Point out each leukocyte.
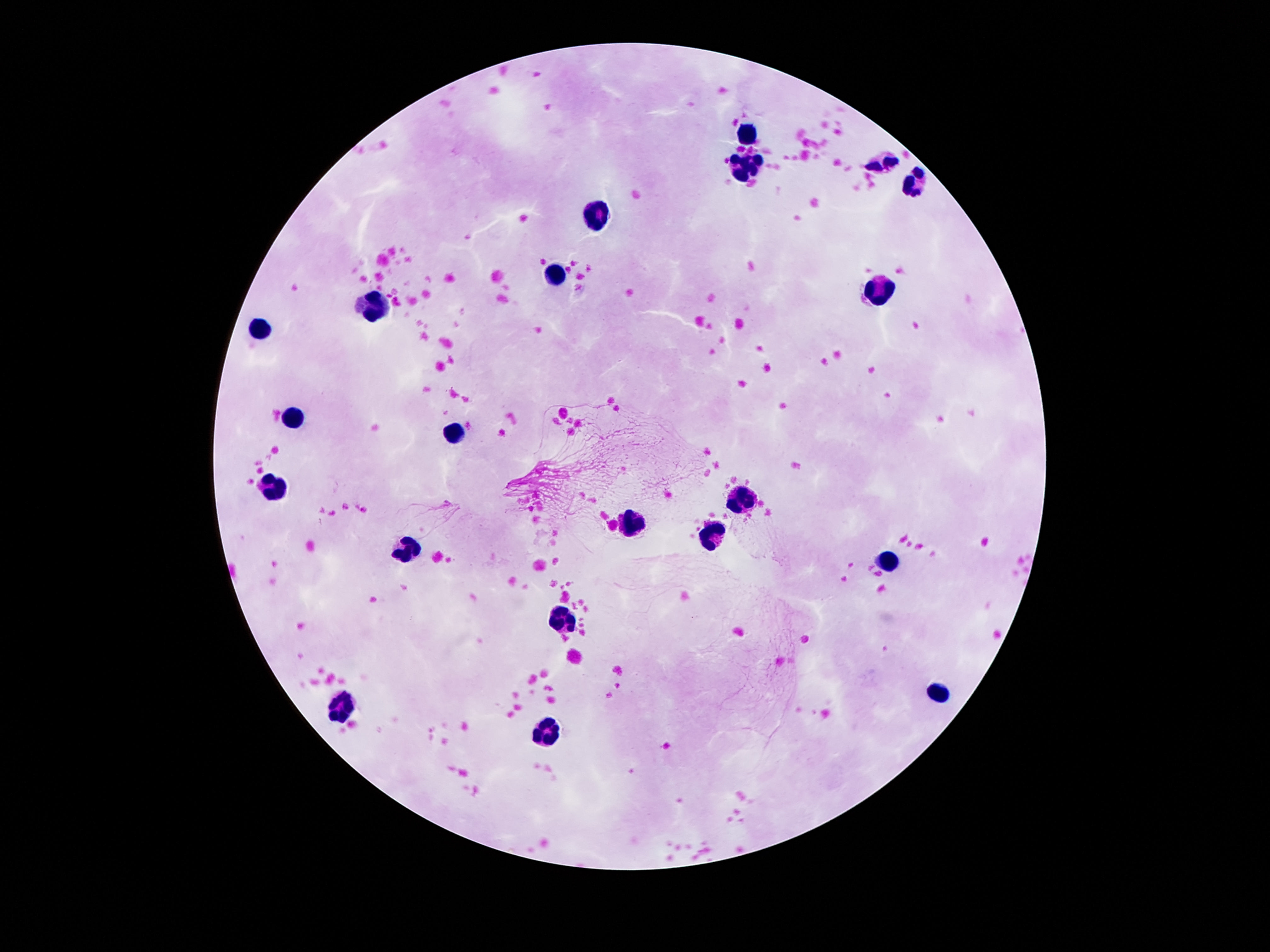

Approximate object centers, in pixels from the top-left corner.
Leukocytes: (x=748, y=135), (x=883, y=163), (x=752, y=167), (x=916, y=183), (x=598, y=212), (x=556, y=274), (x=883, y=287), (x=376, y=305), (x=260, y=327), (x=295, y=419), (x=456, y=433), (x=277, y=486), (x=743, y=499), (x=631, y=523), (x=712, y=534), (x=410, y=552), (x=887, y=564), (x=562, y=618), (x=940, y=691), (x=337, y=706), (x=544, y=731).

preparation: thick blood smear
image_size: 1270×952 pixels
magnification: 100x
field_of_view: one from this slide
capture: smartphone camera through the microscope eyepiece
stain: Giemsa
patient_malaria_status: uninfected